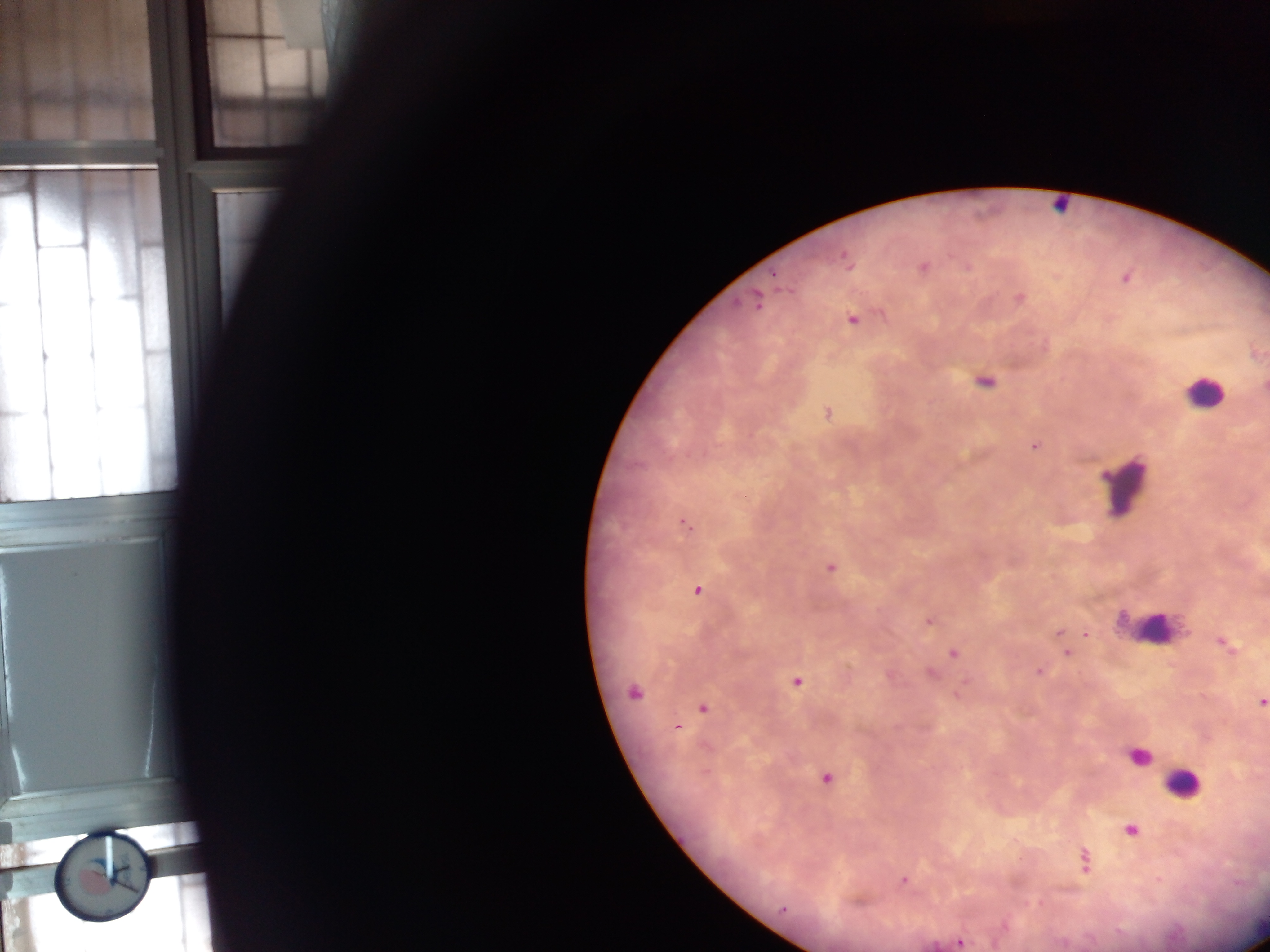
Approximate centers as [x, y] in pixels. Plasmodium parasite locations: [845, 259], [924, 268], [776, 274], [1125, 278], [1019, 298], [757, 301], [852, 319], [984, 382], [1264, 386], [828, 413], [1034, 446], [744, 497], [684, 524], [830, 567], [697, 590], [929, 620], [1059, 632], [1086, 634], [1223, 643], [953, 654], [1066, 654], [1038, 672], [931, 673], [796, 683], [633, 692], [1261, 702], [702, 708], [677, 727], [827, 779], [1131, 831], [1084, 860], [903, 880], [782, 909], [959, 942]. Leukocyte locations: [1060, 206], [1204, 393], [1125, 484], [1151, 623], [1139, 756], [1182, 783]. Thick blood film. One field of view. Image is 1270×952 pixels. Photographed through a microscope with a mobile-phone camera. Sample from Ghana.